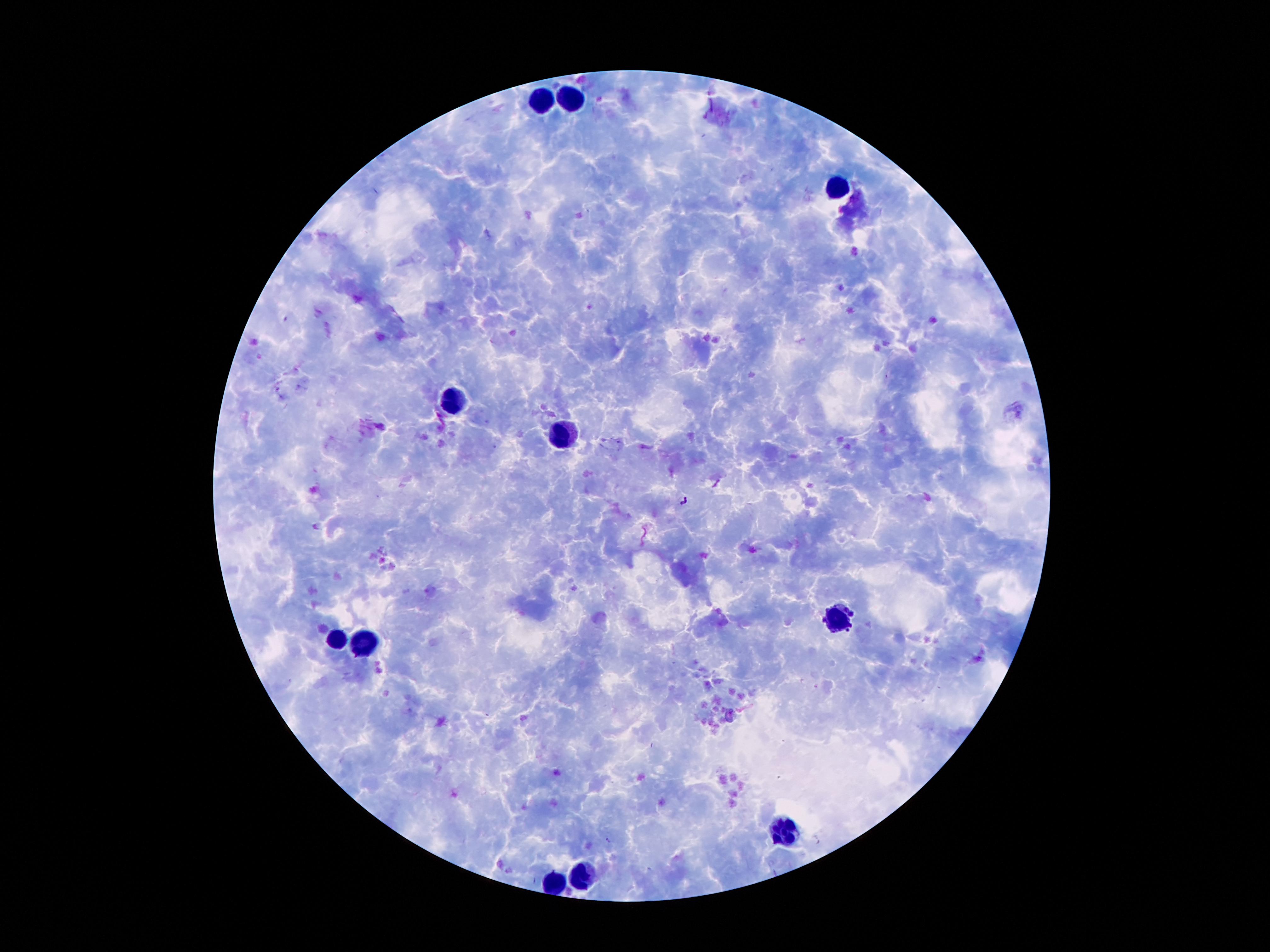
Approximate centers as {x, y} in pixels.
Summary:
  - Leukocyte locations: {577, 100}, {545, 101}, {836, 189}, {451, 399}, {568, 434}, {841, 621}, {335, 639}, {365, 647}, {785, 828}, {582, 877}, {554, 885}
  - Malaria parasite locations: {686, 500}
  - Stain: Giemsa
  - Capture: smartphone camera through the microscope eyepiece
  - Image size: 1270×952 pixels
  - Field of view: single
  - Patient malaria status: positive for Plasmodium falciparum
  - Magnification: 100x
  - Preparation: thick blood film